Outline each blood parasite and name the species.
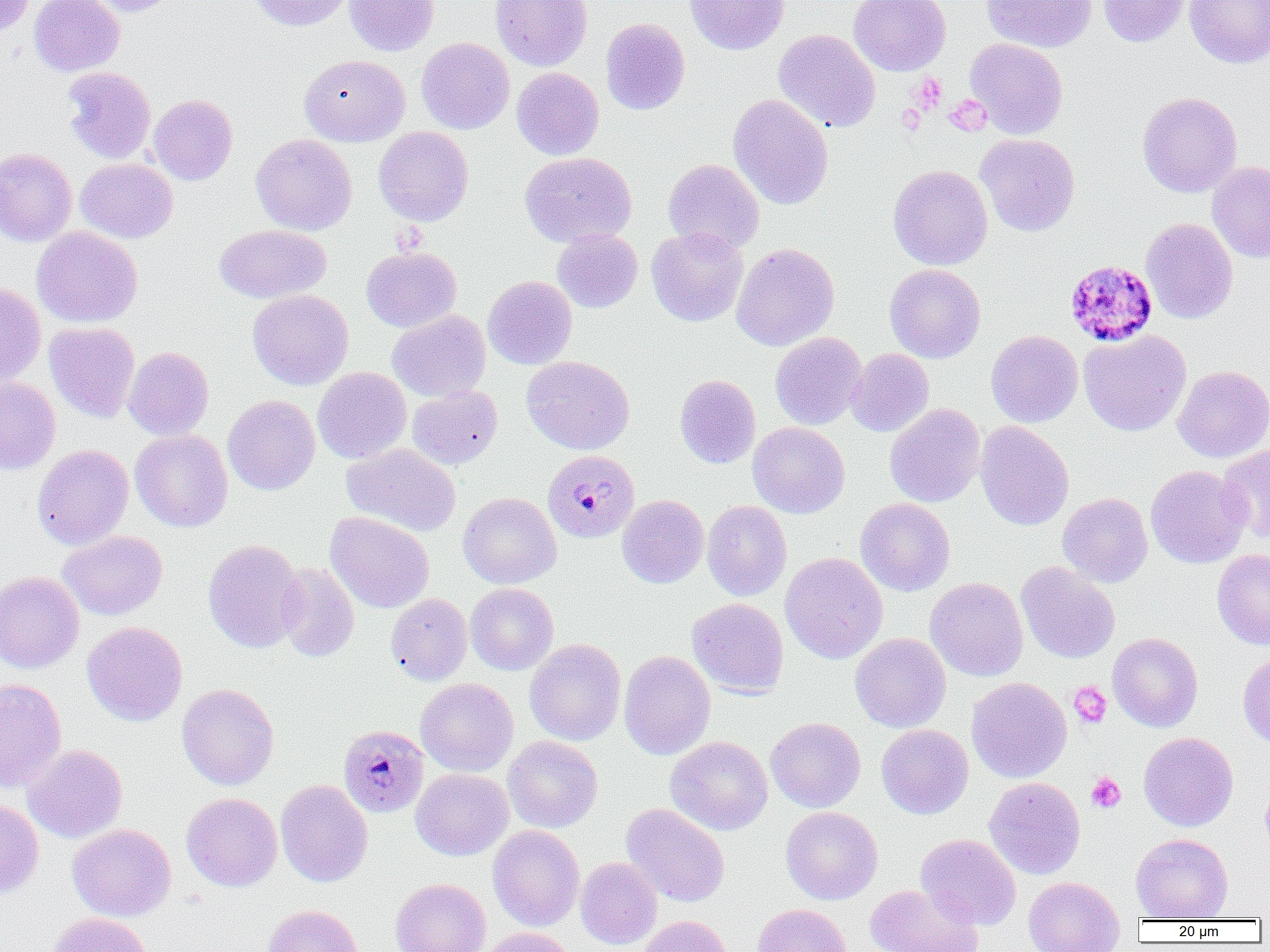

Approximate bounding boxes as (x1, y1, x2, y2) in pixels.
Plasmodium malariae-infected red blood cells: (1064, 259, 1158, 347), (542, 450, 640, 543), (338, 724, 430, 817).
No Plasmodium falciparum, Plasmodium ovale, Plasmodium vivax, Babesia divergens, or Trypanosoma brucei observed.

Uninfected red blood cell locations: (0, 0, 35, 36), (29, 0, 124, 77), (84, 0, 178, 17), (247, 0, 352, 31), (344, 0, 438, 56), (490, 0, 593, 71), (685, 0, 789, 55), (849, 0, 951, 76), (981, 0, 1096, 53), (1097, 0, 1192, 47), (1185, 0, 1270, 68), (600, 18, 690, 115), (773, 29, 880, 132), (416, 37, 514, 134), (965, 38, 1068, 139), (299, 54, 410, 146), (62, 67, 156, 164), (512, 67, 603, 160), (1137, 91, 1242, 197), (148, 94, 237, 185), (727, 94, 834, 210), (373, 126, 474, 226), (251, 134, 357, 235), (976, 134, 1080, 236), (0, 148, 77, 246), (520, 151, 636, 247), (75, 158, 178, 243), (663, 158, 764, 255), (1207, 160, 1270, 263), (888, 165, 993, 270), (1140, 217, 1238, 324), (214, 224, 331, 303), (32, 226, 143, 328), (646, 226, 748, 327), (552, 229, 642, 312), (731, 243, 839, 351), (361, 246, 461, 332), (884, 264, 985, 363), (482, 276, 577, 369), (0, 282, 46, 386), (247, 289, 353, 390), (387, 310, 490, 402), (45, 322, 140, 423), (985, 330, 1083, 427), (1079, 330, 1191, 436), (770, 332, 867, 429), (123, 347, 214, 440), (846, 348, 933, 437), (522, 355, 634, 455), (1173, 365, 1270, 462), (313, 367, 411, 463), (674, 374, 761, 468), (0, 377, 61, 475), (407, 385, 502, 470), (222, 395, 320, 495), (885, 403, 985, 507), (975, 421, 1074, 530), (747, 422, 850, 518), (130, 429, 233, 532), (342, 443, 461, 537), (32, 444, 133, 550), (1217, 444, 1270, 543), (1145, 465, 1251, 568), (458, 492, 561, 589), (1057, 493, 1152, 587), (617, 495, 708, 588), (855, 498, 955, 596), (702, 500, 792, 601), (325, 511, 434, 613), (57, 530, 167, 620), (203, 539, 305, 653), (1212, 549, 1270, 650), (780, 552, 887, 664), (1016, 562, 1120, 663), (275, 563, 359, 662), (0, 571, 84, 673), (926, 577, 1028, 681), (465, 583, 559, 675), (385, 593, 472, 685), (687, 598, 789, 698), (82, 621, 187, 726), (850, 633, 951, 732), (1108, 633, 1203, 732), (525, 639, 626, 745), (618, 650, 715, 759), (1238, 650, 1270, 749), (966, 677, 1072, 783), (0, 678, 66, 793), (416, 678, 518, 777), (177, 683, 279, 790), (766, 717, 866, 812), (876, 724, 973, 819), (1139, 732, 1238, 831), (503, 735, 603, 833), (665, 736, 773, 836), (22, 744, 127, 843), (411, 768, 514, 860), (983, 777, 1085, 879), (1261, 777, 1270, 856), (276, 780, 373, 887), (181, 793, 282, 891), (0, 799, 44, 899), (621, 803, 729, 907), (781, 807, 883, 905), (68, 823, 176, 921), (488, 825, 584, 931), (916, 833, 1021, 930), (1131, 833, 1233, 920), (575, 857, 662, 949), (1024, 876, 1124, 952), (390, 878, 490, 952), (865, 884, 982, 952), (752, 903, 852, 952), (262, 904, 365, 952), (48, 912, 151, 952), (637, 915, 732, 952), (479, 927, 577, 952). Platelet locations: (911, 73, 947, 113), (944, 96, 991, 136), (896, 104, 927, 135), (1069, 681, 1112, 729), (1086, 772, 1126, 813). Slide-level diagnosis: Plasmodium malariae. One field of a larger specimen. Light microscopy. Image is 1270×952 pixels. Captured at 1000x magnification. Thin blood film.